Identify the cell.
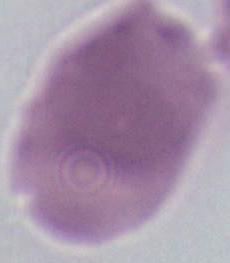
This is an erythrocyte.

Micrograph. 1000x magnification.